Locate every blood parasite and identify its species.
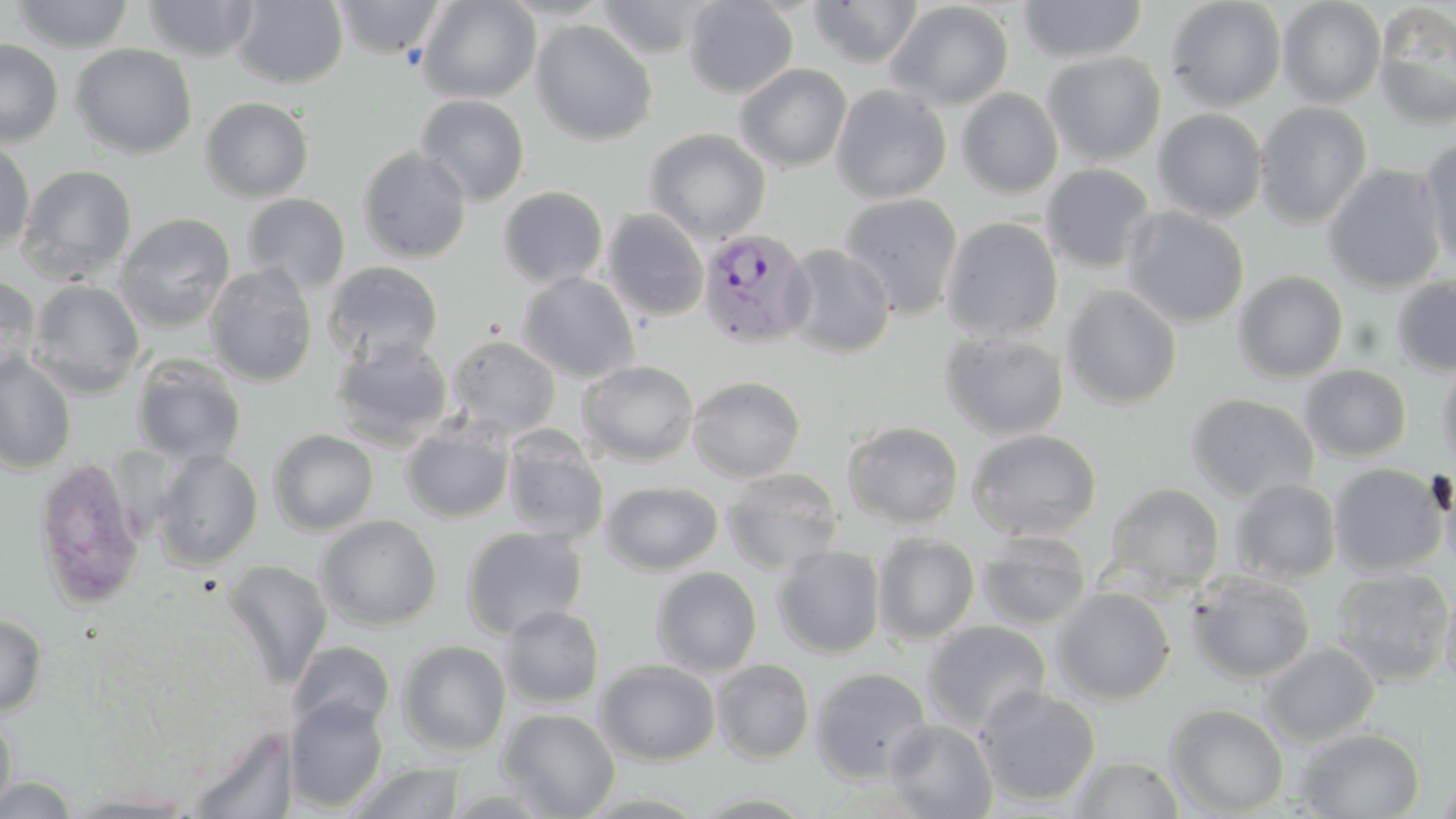

Approximate bounding boxes as (x1,y1)-(x2,y2) corner pairs in pixels.
Plasmodium vivax-infected red blood cells: (697,226)-(816,350).
No Plasmodium falciparum, Plasmodium ovale, Plasmodium malariae, Babesia divergens, or Trypanosoma brucei observed.

Uninfected red blood cell locations: (8,0)-(136,53), (232,0)-(348,89), (417,0)-(541,104), (496,0)-(617,21), (684,0)-(798,98), (807,0)-(924,67), (1016,0)-(1148,63), (1164,0)-(1287,111), (141,1)-(262,61), (332,1)-(447,60), (594,1)-(715,56), (884,1)-(1014,110), (1277,1)-(1386,109), (1372,3)-(1456,129), (530,20)-(658,146), (0,39)-(64,148), (70,43)-(197,159), (1041,51)-(1166,167), (734,63)-(853,172), (830,84)-(951,204), (956,88)-(1064,198), (415,94)-(530,206), (200,97)-(314,203), (1254,101)-(1373,228), (1152,108)-(1268,223), (644,128)-(771,244), (0,138)-(35,255), (1419,138)-(1456,270), (356,147)-(472,263), (16,164)-(138,284), (1040,164)-(1156,274), (1323,164)-(1447,294), (497,186)-(608,289), (241,193)-(351,292), (839,193)-(964,319), (1121,207)-(1249,329), (603,209)-(709,322), (115,213)-(236,332), (940,217)-(1064,341), (782,243)-(896,359), (323,260)-(444,366), (204,262)-(318,387), (1232,271)-(1348,382), (517,272)-(640,383), (0,275)-(42,384), (1390,276)-(1456,377), (27,279)-(145,397), (1062,286)-(1182,409), (939,330)-(1069,439), (330,335)-(454,449), (446,335)-(561,438), (130,354)-(247,467), (0,356)-(77,473), (1436,356)-(1456,476), (577,360)-(699,466), (1299,364)-(1413,462), (687,375)-(805,482), (1185,393)-(1320,503), (400,420)-(514,523), (843,420)-(964,530), (967,428)-(1103,542), (268,429)-(379,536), (502,431)-(609,544), (152,449)-(263,571), (33,455)-(146,610), (1328,462)-(1448,577), (1438,465)-(1456,579), (722,467)-(844,574), (1229,478)-(1341,585), (600,481)-(723,575), (1104,482)-(1225,597), (315,514)-(443,631), (460,526)-(588,640), (976,530)-(1092,630), (873,532)-(980,644), (772,545)-(886,658), (223,559)-(333,687), (1330,566)-(1455,686), (651,567)-(763,677), (1187,571)-(1316,685), (1440,580)-(1456,696), (1051,587)-(1175,704), (499,605)-(605,709), (0,613)-(48,717), (923,620)-(1051,733), (289,640)-(396,736), (397,640)-(512,757), (1260,642)-(1379,746), (595,659)-(721,766), (711,659)-(816,764), (810,667)-(933,784), (975,686)-(1102,807), (285,696)-(390,812), (1165,703)-(1289,816), (497,708)-(620,818), (0,709)-(17,814), (883,717)-(998,819), (187,725)-(298,818), (1294,727)-(1425,818), (1068,754)-(1186,818), (344,762)-(468,819), (1436,768)-(1456,818), (0,774)-(83,817), (63,787)-(201,817), (688,790)-(822,817). Slide-level diagnosis: Plasmodium vivax. One field of a larger specimen. Optical microscopy. May-Grünwald-Giemsa-stained preparation. Thin blood film. 1000x magnification. Image is 1456×819 pixels.